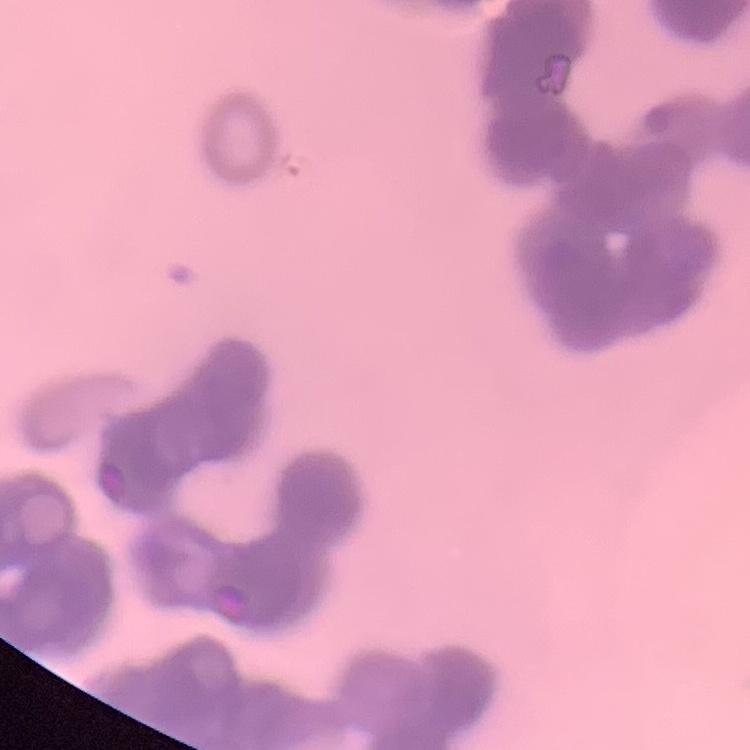

red blood cell morphology = rouleaux formation
preparation = thin blood smear
stain = Field's or Giemsa
image type = square crop of a larger photomicrograph